Give the extent of all Plasmodium falciparum-infected red blood cells.
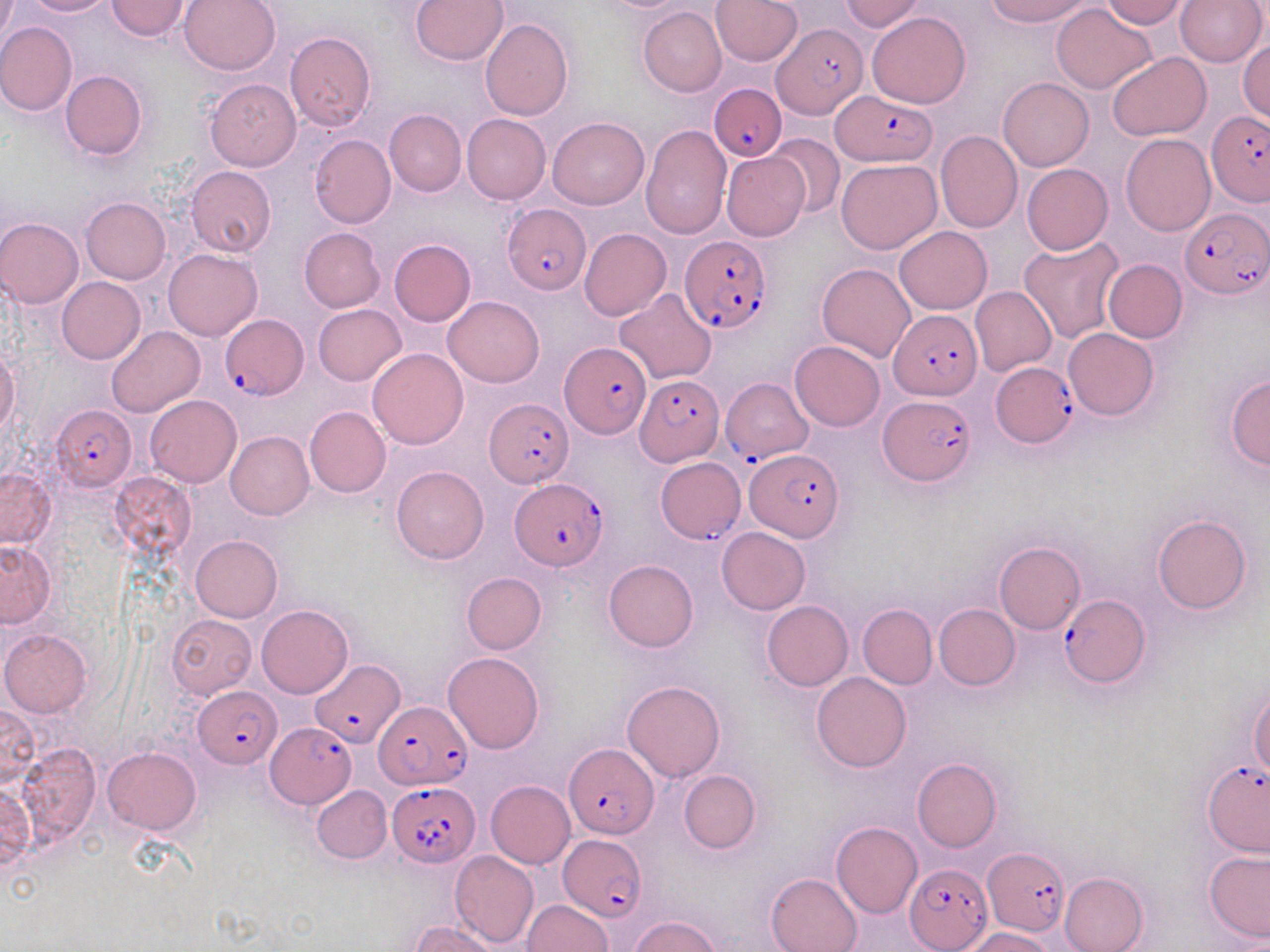
Approximate bounding boxes as named x1/y1/x2/y2 corners in pixels.
Plasmodium falciparum-infected red blood cells: (x1=772, y1=23, x2=862, y2=117), (x1=709, y1=84, x2=786, y2=162), (x1=830, y1=89, x2=936, y2=167), (x1=1207, y1=109, x2=1269, y2=205), (x1=505, y1=203, x2=590, y2=294), (x1=1179, y1=204, x2=1269, y2=298), (x1=679, y1=235, x2=772, y2=336), (x1=888, y1=310, x2=979, y2=401), (x1=219, y1=313, x2=307, y2=399), (x1=560, y1=341, x2=650, y2=438), (x1=994, y1=361, x2=1080, y2=446), (x1=634, y1=373, x2=723, y2=465), (x1=722, y1=377, x2=812, y2=466), (x1=880, y1=394, x2=974, y2=485), (x1=486, y1=397, x2=573, y2=487), (x1=51, y1=407, x2=137, y2=491), (x1=745, y1=450, x2=844, y2=542), (x1=655, y1=457, x2=747, y2=543), (x1=509, y1=477, x2=608, y2=572), (x1=1058, y1=594, x2=1150, y2=688), (x1=311, y1=661, x2=403, y2=747), (x1=194, y1=685, x2=280, y2=769), (x1=374, y1=702, x2=471, y2=787), (x1=267, y1=725, x2=355, y2=808), (x1=565, y1=744, x2=658, y2=841), (x1=1203, y1=761, x2=1269, y2=856), (x1=387, y1=781, x2=481, y2=866), (x1=558, y1=836, x2=649, y2=919), (x1=983, y1=848, x2=1069, y2=937), (x1=907, y1=864, x2=990, y2=948).

Summary:
  - Uninfected red blood cell locations: (x1=0, y1=0, x2=21, y2=66), (x1=22, y1=0, x2=114, y2=16), (x1=179, y1=0, x2=281, y2=76), (x1=411, y1=0, x2=509, y2=66), (x1=711, y1=0, x2=803, y2=67), (x1=838, y1=0, x2=927, y2=32), (x1=983, y1=0, x2=1094, y2=25), (x1=1100, y1=0, x2=1188, y2=27), (x1=1175, y1=0, x2=1268, y2=67), (x1=107, y1=1, x2=191, y2=41), (x1=1052, y1=4, x2=1157, y2=94), (x1=638, y1=7, x2=727, y2=97), (x1=867, y1=11, x2=970, y2=109), (x1=480, y1=18, x2=574, y2=120), (x1=0, y1=21, x2=77, y2=114), (x1=285, y1=32, x2=376, y2=131), (x1=1238, y1=40, x2=1269, y2=122), (x1=1107, y1=52, x2=1212, y2=140), (x1=60, y1=70, x2=146, y2=160), (x1=997, y1=77, x2=1093, y2=170), (x1=204, y1=78, x2=300, y2=171), (x1=383, y1=110, x2=466, y2=197), (x1=462, y1=114, x2=551, y2=203), (x1=547, y1=115, x2=649, y2=210), (x1=641, y1=124, x2=733, y2=240), (x1=935, y1=130, x2=1023, y2=233), (x1=766, y1=133, x2=846, y2=219), (x1=1120, y1=133, x2=1215, y2=236), (x1=309, y1=134, x2=396, y2=228), (x1=721, y1=151, x2=810, y2=241), (x1=836, y1=158, x2=941, y2=254), (x1=1021, y1=163, x2=1112, y2=255), (x1=185, y1=166, x2=276, y2=257), (x1=80, y1=198, x2=170, y2=284), (x1=0, y1=216, x2=83, y2=308), (x1=894, y1=226, x2=992, y2=314), (x1=299, y1=227, x2=386, y2=312), (x1=580, y1=229, x2=671, y2=321), (x1=1019, y1=237, x2=1124, y2=344), (x1=389, y1=239, x2=475, y2=326), (x1=163, y1=248, x2=262, y2=340), (x1=1103, y1=259, x2=1187, y2=342), (x1=817, y1=263, x2=915, y2=361), (x1=57, y1=277, x2=145, y2=364), (x1=970, y1=287, x2=1056, y2=375), (x1=613, y1=288, x2=716, y2=384), (x1=443, y1=297, x2=544, y2=387), (x1=313, y1=304, x2=406, y2=386), (x1=106, y1=326, x2=204, y2=417), (x1=1063, y1=328, x2=1158, y2=420), (x1=790, y1=340, x2=885, y2=431), (x1=0, y1=347, x2=21, y2=438), (x1=368, y1=348, x2=468, y2=450), (x1=1225, y1=375, x2=1270, y2=471), (x1=145, y1=394, x2=242, y2=487), (x1=304, y1=405, x2=391, y2=498), (x1=225, y1=431, x2=314, y2=520), (x1=391, y1=465, x2=489, y2=564), (x1=0, y1=468, x2=54, y2=548), (x1=108, y1=472, x2=197, y2=560), (x1=1152, y1=515, x2=1251, y2=615), (x1=717, y1=526, x2=811, y2=613), (x1=190, y1=535, x2=282, y2=622), (x1=0, y1=540, x2=56, y2=628), (x1=994, y1=541, x2=1085, y2=634), (x1=604, y1=559, x2=698, y2=652), (x1=461, y1=572, x2=547, y2=654), (x1=761, y1=600, x2=853, y2=691), (x1=256, y1=604, x2=353, y2=698), (x1=858, y1=604, x2=937, y2=689), (x1=933, y1=604, x2=1020, y2=690), (x1=770, y1=606, x2=931, y2=701), (x1=166, y1=613, x2=257, y2=700), (x1=0, y1=629, x2=91, y2=717), (x1=443, y1=652, x2=544, y2=753), (x1=812, y1=672, x2=911, y2=772), (x1=622, y1=680, x2=725, y2=782), (x1=1248, y1=687, x2=1269, y2=778), (x1=0, y1=700, x2=39, y2=791), (x1=15, y1=746, x2=101, y2=846), (x1=102, y1=747, x2=201, y2=833), (x1=912, y1=758, x2=1001, y2=852), (x1=679, y1=769, x2=760, y2=853), (x1=485, y1=779, x2=574, y2=869), (x1=312, y1=784, x2=392, y2=862), (x1=0, y1=785, x2=34, y2=869), (x1=831, y1=821, x2=922, y2=918), (x1=1204, y1=849, x2=1270, y2=944), (x1=450, y1=851, x2=540, y2=947), (x1=1059, y1=871, x2=1149, y2=952), (x1=765, y1=873, x2=863, y2=952), (x1=523, y1=899, x2=612, y2=951), (x1=629, y1=915, x2=725, y2=952), (x1=412, y1=919, x2=502, y2=952), (x1=962, y1=927, x2=1053, y2=952)
  - Slide-level diagnosis: Plasmodium falciparum
  - Image size: 1270×952 pixels
  - Modality: light microscopy
  - Stain: May-Grünwald-Giemsa
  - Field of view: one of a larger specimen
  - Magnification: 1000x
  - Preparation: thin blood film